Outline each uninfected red blood cell.
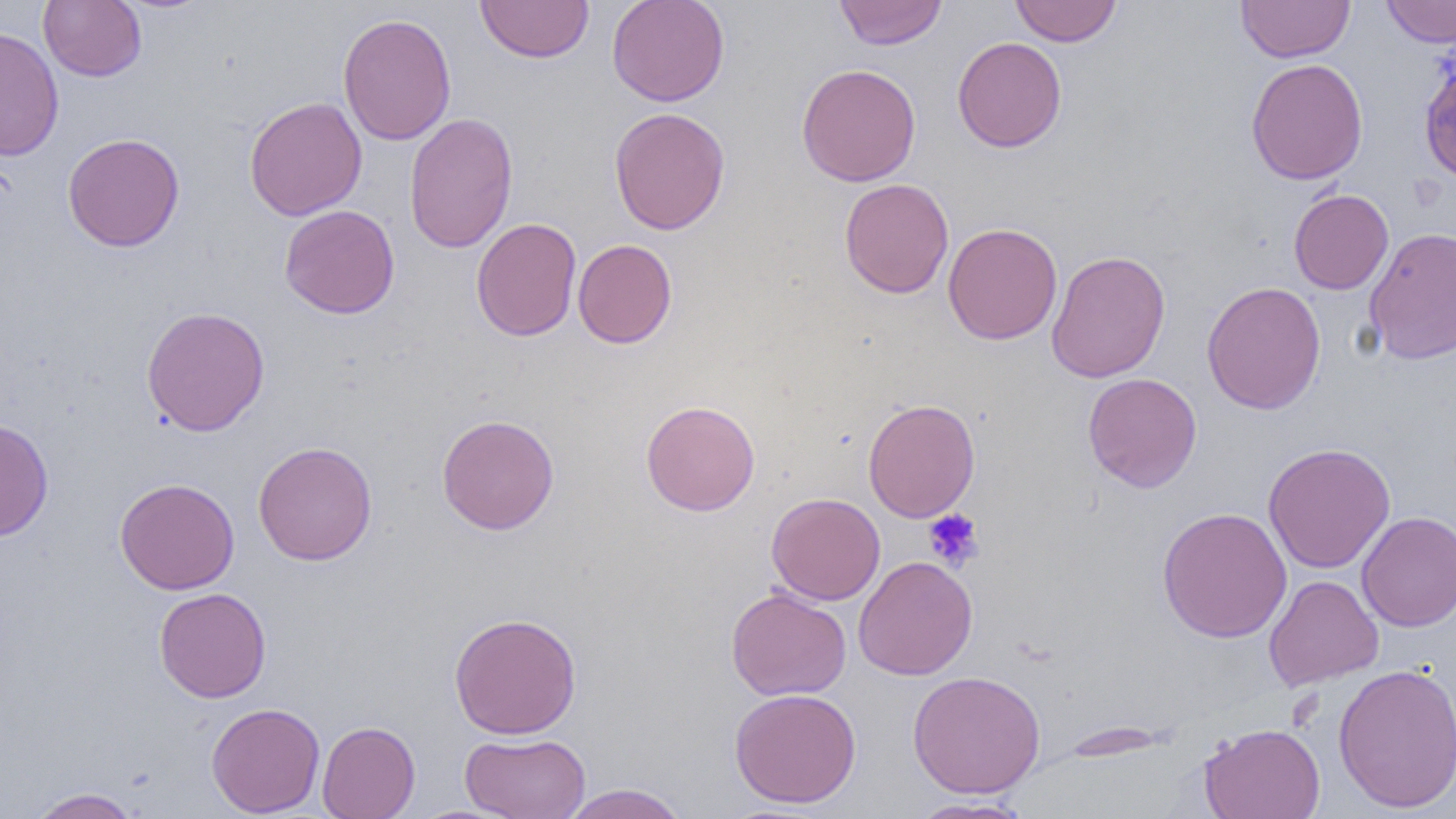
Approximate bounding boxes as (x1, y1, x2, y2) in pixels.
Uninfected red blood cells: (39, 0, 146, 81), (476, 0, 594, 63), (606, 0, 730, 107), (834, 0, 947, 50), (1010, 0, 1123, 46), (1236, 1, 1355, 63), (1381, 1, 1456, 47), (338, 13, 457, 146), (0, 26, 65, 160), (952, 36, 1067, 153), (1246, 58, 1368, 184), (1419, 59, 1456, 185), (796, 63, 921, 187), (244, 96, 368, 221), (608, 107, 731, 235), (404, 112, 519, 254), (62, 132, 185, 252), (839, 178, 954, 298), (1288, 189, 1394, 294), (279, 205, 400, 319), (470, 218, 582, 342), (942, 222, 1063, 345), (1364, 226, 1456, 364), (573, 239, 677, 349), (1046, 249, 1171, 383), (1201, 280, 1327, 415), (140, 306, 270, 437), (1082, 373, 1202, 493), (863, 398, 981, 522), (640, 399, 760, 516), (436, 413, 560, 535), (0, 418, 54, 541), (253, 441, 378, 565), (1263, 442, 1396, 574), (114, 477, 240, 595), (766, 492, 886, 605), (1156, 506, 1292, 644), (1357, 511, 1456, 631), (853, 556, 978, 680), (1264, 575, 1383, 690), (153, 587, 271, 703), (726, 587, 852, 700), (448, 612, 582, 739), (1332, 662, 1456, 814), (907, 670, 1046, 798), (729, 688, 862, 808), (206, 702, 325, 817), (317, 720, 420, 819), (1199, 722, 1326, 819), (460, 732, 591, 819), (560, 783, 691, 819), (26, 788, 144, 818), (906, 797, 1034, 818).

slide-level diagnosis = negative for blood parasites
platelet locations = approximate bounding boxes as (x1, y1, x2, y2) in pixels: (923, 508, 985, 570)
magnification = 1000x
modality = light microscopy
preparation = thin blood smear
image size = 1456×819 pixels
field of view = single